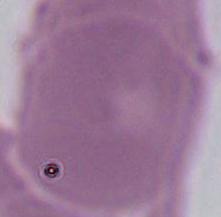

modality: micrograph
identification: erythrocyte
magnification: 1000x